Locate and identify every blood parasite.
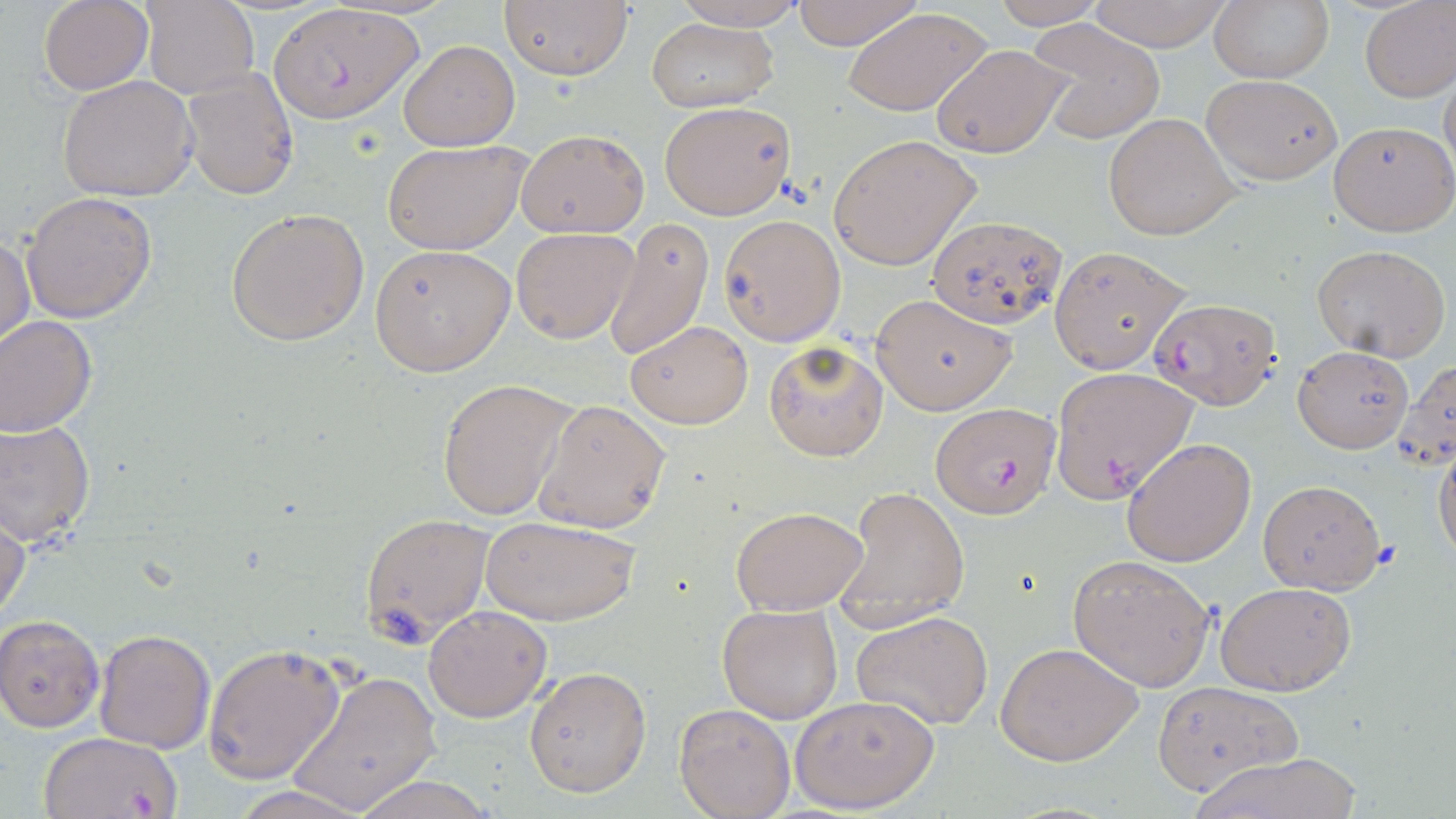
Approximate bounding boxes as named x1/y1/x2/y2 corners in pixels.
Plasmodium falciparum-infected red blood cells: (x1=271, y1=4, x2=423, y2=124), (x1=1148, y1=295, x2=1281, y2=411), (x1=1048, y1=366, x2=1198, y2=503), (x1=932, y1=401, x2=1062, y2=518), (x1=36, y1=732, x2=180, y2=819).
No Plasmodium ovale, Plasmodium malariae, Plasmodium vivax, Babesia divergens, or Trypanosoma brucei observed.

Summary:
  - Uninfected red blood cell locations: (x1=667, y1=0, x2=810, y2=29), (x1=790, y1=0, x2=926, y2=51), (x1=989, y1=0, x2=1114, y2=28), (x1=1084, y1=0, x2=1233, y2=50), (x1=37, y1=1, x2=153, y2=93), (x1=142, y1=1, x2=259, y2=99), (x1=500, y1=1, x2=633, y2=81), (x1=1206, y1=1, x2=1335, y2=84), (x1=1360, y1=1, x2=1455, y2=102), (x1=842, y1=7, x2=993, y2=117), (x1=1027, y1=19, x2=1166, y2=145), (x1=646, y1=20, x2=777, y2=111), (x1=398, y1=40, x2=520, y2=151), (x1=931, y1=42, x2=1074, y2=159), (x1=1439, y1=63, x2=1456, y2=190), (x1=179, y1=68, x2=300, y2=200), (x1=1202, y1=74, x2=1342, y2=183), (x1=56, y1=75, x2=200, y2=201), (x1=659, y1=102, x2=795, y2=221), (x1=1104, y1=112, x2=1240, y2=240), (x1=1327, y1=121, x2=1455, y2=237), (x1=515, y1=129, x2=649, y2=238), (x1=828, y1=135, x2=981, y2=271), (x1=384, y1=140, x2=527, y2=255), (x1=23, y1=190, x2=156, y2=323), (x1=225, y1=208, x2=370, y2=346), (x1=927, y1=213, x2=1066, y2=329), (x1=719, y1=215, x2=845, y2=345), (x1=603, y1=218, x2=714, y2=362), (x1=510, y1=226, x2=641, y2=344), (x1=0, y1=233, x2=35, y2=351), (x1=369, y1=244, x2=516, y2=376), (x1=1311, y1=244, x2=1452, y2=362), (x1=1048, y1=246, x2=1189, y2=374), (x1=870, y1=292, x2=1018, y2=415), (x1=0, y1=316, x2=97, y2=437), (x1=624, y1=320, x2=754, y2=429), (x1=763, y1=340, x2=890, y2=461), (x1=1293, y1=346, x2=1413, y2=453), (x1=1395, y1=358, x2=1456, y2=473), (x1=436, y1=379, x2=575, y2=520), (x1=532, y1=399, x2=670, y2=532), (x1=0, y1=420, x2=96, y2=546), (x1=1434, y1=437, x2=1456, y2=568), (x1=1122, y1=438, x2=1257, y2=568), (x1=1256, y1=479, x2=1387, y2=595), (x1=833, y1=486, x2=970, y2=633), (x1=731, y1=505, x2=870, y2=615), (x1=358, y1=512, x2=495, y2=643), (x1=0, y1=513, x2=28, y2=627), (x1=481, y1=515, x2=640, y2=626), (x1=1066, y1=552, x2=1216, y2=690), (x1=1216, y1=582, x2=1356, y2=696), (x1=717, y1=603, x2=842, y2=723), (x1=423, y1=605, x2=553, y2=722), (x1=852, y1=610, x2=994, y2=732), (x1=0, y1=614, x2=105, y2=732), (x1=94, y1=630, x2=215, y2=753), (x1=203, y1=642, x2=347, y2=784), (x1=995, y1=642, x2=1144, y2=766), (x1=523, y1=665, x2=652, y2=798), (x1=286, y1=669, x2=440, y2=814), (x1=1151, y1=681, x2=1302, y2=794), (x1=788, y1=694, x2=938, y2=813), (x1=673, y1=702, x2=796, y2=819), (x1=1187, y1=753, x2=1365, y2=818), (x1=348, y1=775, x2=498, y2=819), (x1=224, y1=784, x2=378, y2=819)
  - Slide-level diagnosis: Plasmodium falciparum
  - Field of view: single
  - Modality: light microscopy
  - Stain: May-Grünwald-Giemsa
  - Magnification: 1000x
  - Image size: 1456×819 pixels
  - Preparation: thin blood smear